Assess the morphology of the red blood cells.
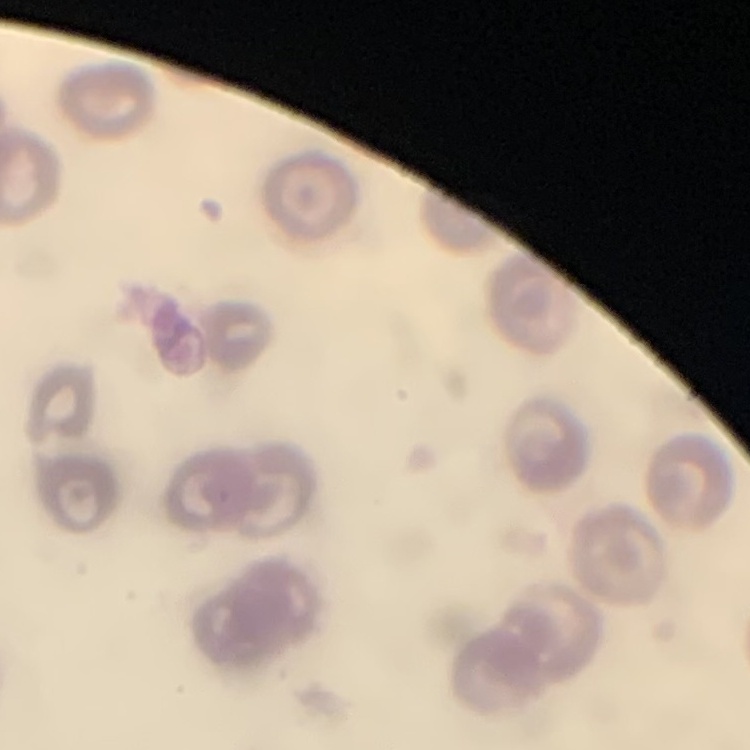

No rouleaux formation.

Summary:
  - Preparation: thin blood film
  - Stain: Field's or Giemsa
  - Image type: square crop of a larger photomicrograph